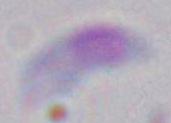
modality = photomicrograph
magnification = 1000x
identification = Toxoplasma gondii